Outline platelets.
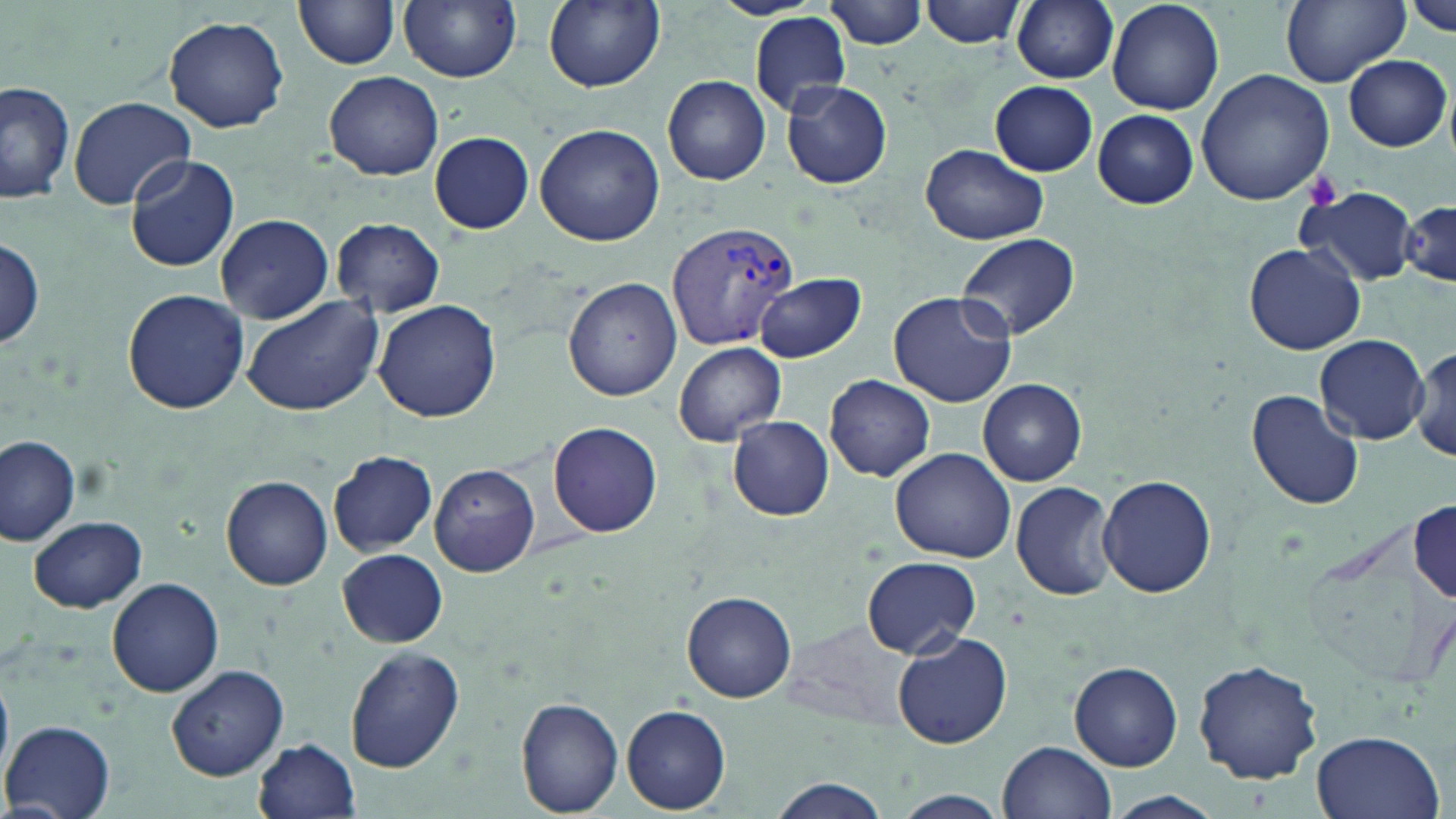
Approximate bounding boxes as named x1/y1/x2/y2 corners in pixels.
Platelets: (x1=1305, y1=174, x2=1341, y2=211).

Plasmodium vivax-infected red blood cell locations: (x1=667, y1=220, x2=800, y2=353). Uninfected red blood cell locations: (x1=399, y1=0, x2=521, y2=82), (x1=543, y1=0, x2=665, y2=91), (x1=710, y1=0, x2=825, y2=19), (x1=919, y1=0, x2=1025, y2=48), (x1=1004, y1=0, x2=1112, y2=171), (x1=1011, y1=0, x2=1119, y2=84), (x1=1107, y1=0, x2=1224, y2=115), (x1=1279, y1=0, x2=1408, y2=86), (x1=297, y1=1, x2=400, y2=71), (x1=827, y1=1, x2=930, y2=49), (x1=1408, y1=1, x2=1455, y2=36), (x1=751, y1=13, x2=851, y2=114), (x1=163, y1=14, x2=290, y2=133), (x1=1344, y1=55, x2=1451, y2=151), (x1=323, y1=70, x2=444, y2=181), (x1=1196, y1=70, x2=1336, y2=207), (x1=663, y1=75, x2=770, y2=185), (x1=1, y1=79, x2=76, y2=206), (x1=782, y1=80, x2=892, y2=190), (x1=990, y1=81, x2=1098, y2=175), (x1=68, y1=97, x2=195, y2=209), (x1=1093, y1=110, x2=1198, y2=207), (x1=534, y1=123, x2=664, y2=246), (x1=430, y1=131, x2=534, y2=234), (x1=919, y1=145, x2=1049, y2=246), (x1=125, y1=155, x2=240, y2=273), (x1=1296, y1=186, x2=1419, y2=287), (x1=1399, y1=193, x2=1455, y2=291), (x1=216, y1=214, x2=334, y2=323), (x1=332, y1=218, x2=445, y2=318), (x1=957, y1=232, x2=1079, y2=341), (x1=0, y1=236, x2=46, y2=351), (x1=1244, y1=244, x2=1364, y2=355), (x1=754, y1=274, x2=864, y2=363), (x1=564, y1=277, x2=682, y2=402), (x1=122, y1=288, x2=250, y2=414), (x1=888, y1=290, x2=1017, y2=407), (x1=241, y1=296, x2=385, y2=416), (x1=372, y1=299, x2=503, y2=423), (x1=1315, y1=334, x2=1428, y2=444), (x1=674, y1=341, x2=785, y2=446), (x1=1412, y1=343, x2=1456, y2=463), (x1=685, y1=352, x2=813, y2=506), (x1=826, y1=375, x2=935, y2=482), (x1=978, y1=378, x2=1087, y2=486), (x1=1245, y1=387, x2=1366, y2=513), (x1=727, y1=416, x2=834, y2=521), (x1=548, y1=421, x2=663, y2=537), (x1=0, y1=435, x2=81, y2=548), (x1=890, y1=447, x2=1018, y2=564), (x1=329, y1=450, x2=438, y2=556), (x1=428, y1=464, x2=539, y2=576), (x1=1098, y1=474, x2=1215, y2=599), (x1=222, y1=475, x2=333, y2=590), (x1=1010, y1=480, x2=1122, y2=601), (x1=1411, y1=495, x2=1455, y2=600), (x1=28, y1=514, x2=146, y2=612), (x1=1300, y1=514, x2=1440, y2=694), (x1=336, y1=547, x2=447, y2=648), (x1=861, y1=556, x2=983, y2=657), (x1=106, y1=577, x2=226, y2=697), (x1=682, y1=590, x2=797, y2=703), (x1=892, y1=632, x2=1013, y2=749), (x1=344, y1=645, x2=465, y2=772), (x1=1194, y1=658, x2=1324, y2=786), (x1=1070, y1=660, x2=1183, y2=770), (x1=165, y1=664, x2=290, y2=782), (x1=1, y1=673, x2=13, y2=787), (x1=515, y1=696, x2=625, y2=816), (x1=622, y1=704, x2=731, y2=813), (x1=4, y1=721, x2=116, y2=818), (x1=1311, y1=730, x2=1444, y2=819), (x1=253, y1=737, x2=361, y2=817), (x1=997, y1=741, x2=1116, y2=819), (x1=766, y1=780, x2=891, y2=818), (x1=887, y1=790, x2=1011, y2=819), (x1=1103, y1=791, x2=1223, y2=819). Slide-level diagnosis: Plasmodium vivax. Image is 1456×819 pixels. One field of a larger specimen. Thin blood film. May-Grünwald-Giemsa stain. Captured at 1000x magnification. Optical microscopy.